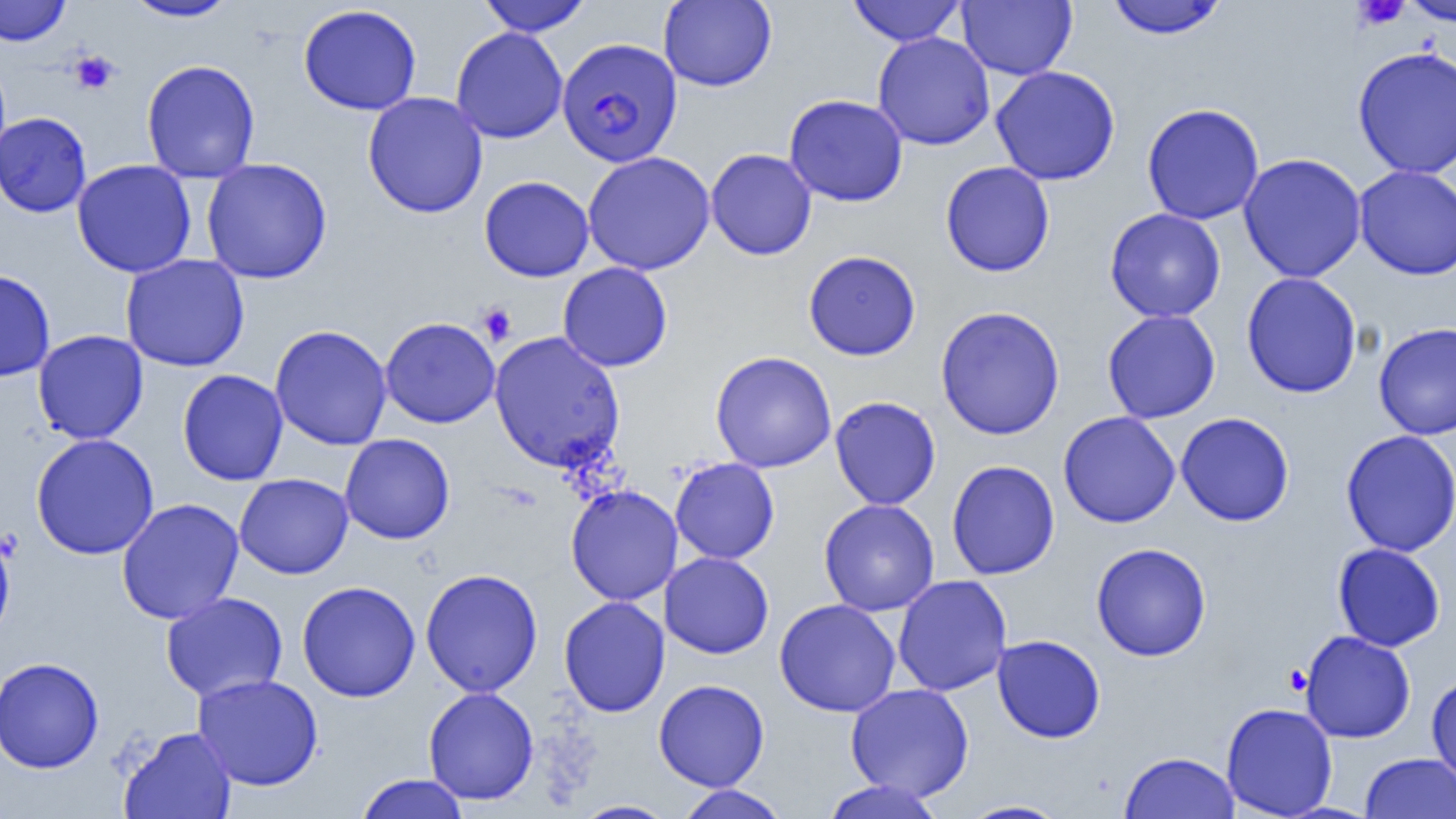

slide-level diagnosis = Plasmodium falciparum
magnification = 1000x
platelet locations = approximate bounding boxes as [x1, y1, x2, y2] in pixels: [1351, 0, 1410, 31], [69, 50, 119, 94], [476, 302, 517, 346], [1284, 665, 1312, 695]
image size = 1456×819 pixels
Plasmodium falciparum-infected red blood cell locations = approximate bounding boxes as [x1, y1, x2, y2] in pixels: [556, 38, 683, 168]
field of view = one of a larger specimen
modality = light microscopy
uninfected red blood cell locations = approximate bounding boxes as [x1, y1, x2, y2] in pixels: [0, 0, 71, 46], [123, 0, 240, 22], [476, 0, 592, 36], [658, 0, 777, 92], [847, 0, 965, 46], [1400, 0, 1456, 27], [957, 1, 1077, 80], [1105, 1, 1229, 39], [298, 4, 422, 115], [450, 26, 568, 144], [872, 32, 995, 150], [1352, 46, 1456, 178], [141, 59, 260, 183], [990, 66, 1121, 186], [362, 92, 488, 218], [784, 94, 908, 207], [1142, 103, 1265, 225], [0, 112, 92, 217], [705, 148, 817, 261], [583, 151, 715, 275], [1238, 153, 1367, 283], [201, 157, 332, 284], [72, 159, 197, 278], [940, 161, 1055, 277], [1353, 165, 1456, 280], [479, 175, 594, 282], [1104, 208, 1226, 323], [803, 250, 921, 361], [120, 253, 250, 372], [557, 262, 673, 372], [0, 269, 56, 382], [1241, 271, 1363, 399], [935, 305, 1066, 440], [1102, 309, 1221, 424], [379, 317, 500, 428], [1373, 321, 1456, 440], [270, 325, 392, 450], [32, 329, 148, 444], [489, 331, 626, 473], [710, 351, 836, 472], [177, 369, 288, 486], [830, 395, 941, 510], [1058, 411, 1181, 528], [1175, 411, 1295, 526], [1340, 430, 1456, 557], [30, 433, 159, 560], [340, 433, 455, 544], [670, 458, 780, 564], [946, 460, 1060, 580], [234, 473, 353, 579], [566, 484, 683, 606], [117, 498, 244, 625], [818, 499, 939, 616], [0, 525, 15, 643], [1090, 542, 1212, 661], [1332, 543, 1446, 651], [660, 552, 774, 658], [420, 568, 543, 697], [893, 575, 1012, 697], [297, 580, 421, 702], [160, 591, 289, 702], [559, 596, 670, 717], [774, 598, 901, 717], [1299, 630, 1416, 743], [992, 634, 1106, 743], [1, 656, 104, 774], [192, 673, 324, 791], [1426, 674, 1456, 786], [654, 679, 769, 791], [845, 683, 974, 801], [423, 686, 539, 805], [1221, 702, 1338, 819], [117, 726, 237, 818], [1120, 751, 1239, 818], [1360, 753, 1456, 818], [355, 774, 469, 819], [820, 779, 946, 819], [673, 785, 789, 819], [571, 800, 678, 819], [958, 800, 1071, 818]
preparation = thin blood smear